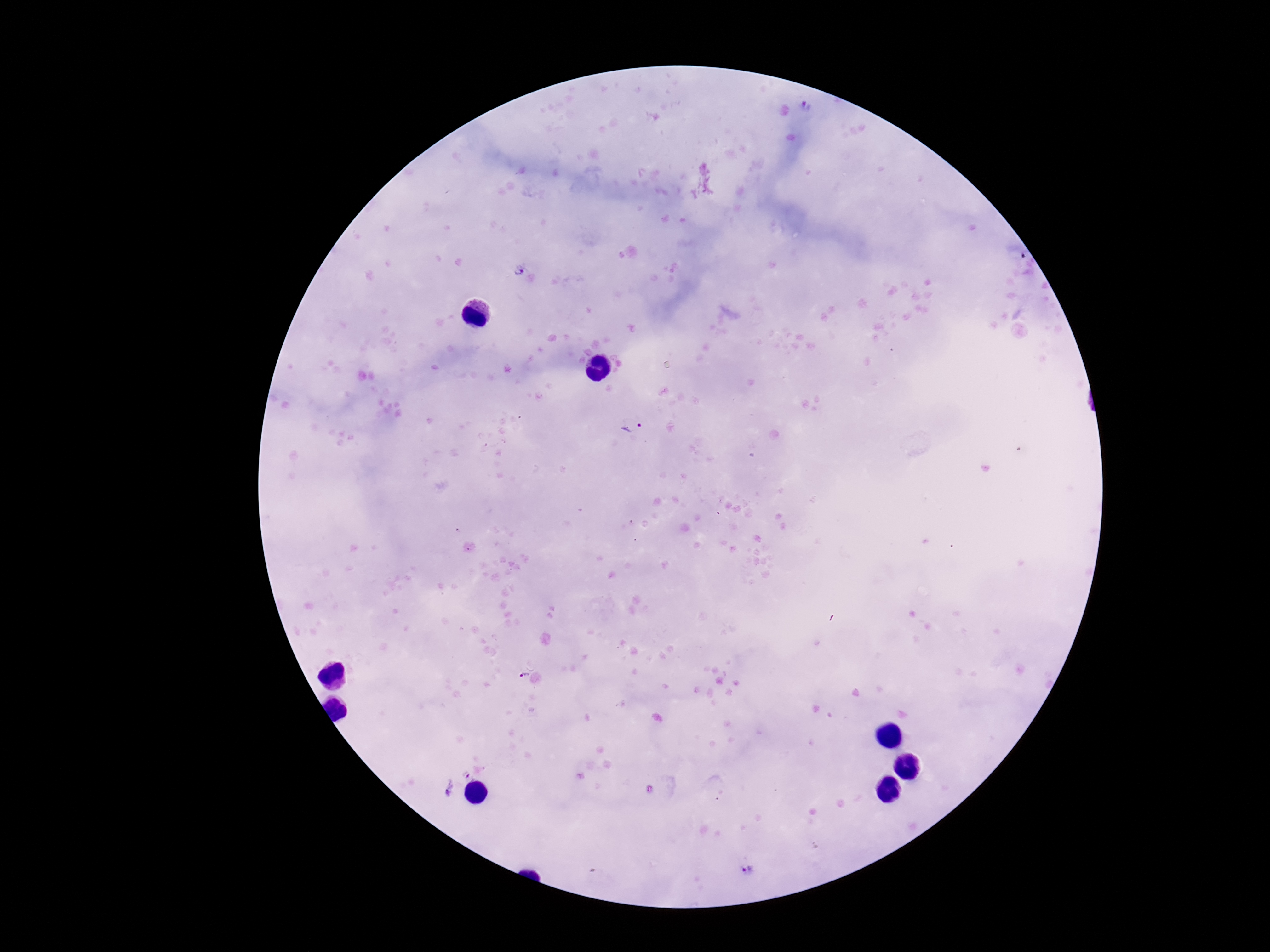
Plasmodium parasite locations = approximate object centers, in pixels from the top-left corner: (x=806, y=107), (x=518, y=271), (x=634, y=428), (x=522, y=675), (x=466, y=775), (x=449, y=793), (x=748, y=870)
preparation = thick blood smear
patient malaria status = positive
image size = 1270×952 pixels
stain = Giemsa
field of view = one from this slide
capture = smartphone camera through the microscope eyepiece
magnification = 100x